Outline each Plasmodium ovale-infected red blood cell.
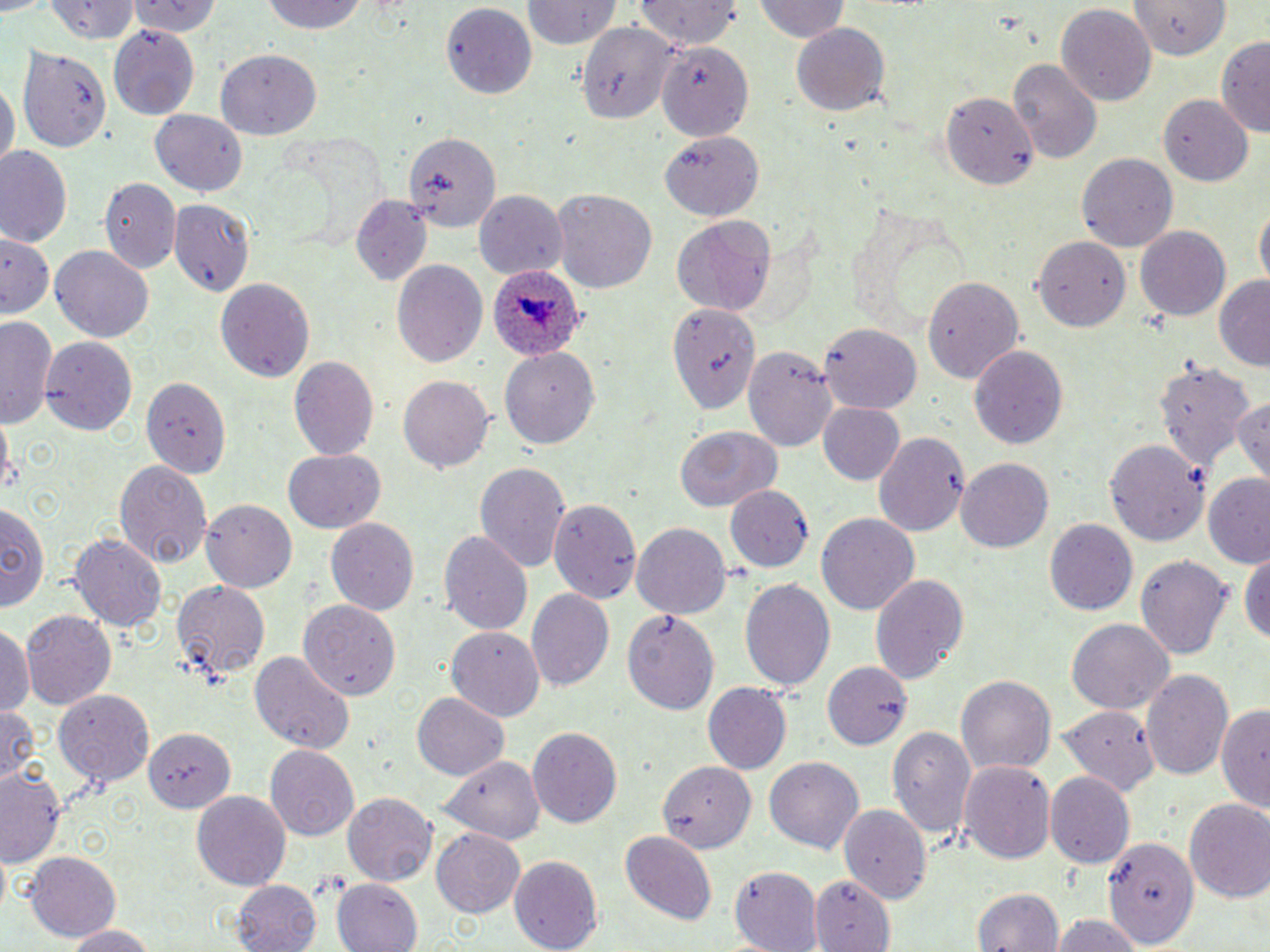
Approximate bounding boxes as named x1/y1/x2/y2 corners in pixels.
Plasmodium ovale-infected red blood cells: (x1=484, y1=264, x2=585, y2=363).

slide-level diagnosis = Plasmodium ovale
magnification = 1000x
field of view = one of a larger specimen
uninfected red blood cell locations = approximate bounding boxes as named x1/y1/x2/y2 corners in pixels: (x1=127, y1=0, x2=221, y2=37), (x1=257, y1=0, x2=371, y2=36), (x1=637, y1=0, x2=742, y2=49), (x1=754, y1=0, x2=849, y2=44), (x1=45, y1=1, x2=141, y2=44), (x1=518, y1=1, x2=622, y2=48), (x1=441, y1=3, x2=535, y2=101), (x1=1127, y1=3, x2=1233, y2=57), (x1=1055, y1=4, x2=1157, y2=103), (x1=577, y1=21, x2=677, y2=127), (x1=790, y1=21, x2=890, y2=115), (x1=107, y1=25, x2=200, y2=121), (x1=1216, y1=33, x2=1270, y2=138), (x1=656, y1=34, x2=758, y2=141), (x1=19, y1=41, x2=116, y2=152), (x1=215, y1=50, x2=319, y2=135), (x1=1009, y1=57, x2=1102, y2=164), (x1=1, y1=79, x2=15, y2=175), (x1=941, y1=92, x2=1036, y2=185), (x1=1159, y1=95, x2=1253, y2=185), (x1=151, y1=109, x2=246, y2=195), (x1=403, y1=131, x2=499, y2=234), (x1=659, y1=132, x2=762, y2=219), (x1=660, y1=134, x2=762, y2=223), (x1=1, y1=148, x2=73, y2=248), (x1=1077, y1=153, x2=1179, y2=252), (x1=100, y1=176, x2=182, y2=274), (x1=551, y1=189, x2=658, y2=294), (x1=474, y1=193, x2=565, y2=279), (x1=351, y1=194, x2=430, y2=285), (x1=170, y1=199, x2=257, y2=298), (x1=1255, y1=203, x2=1268, y2=292), (x1=672, y1=216, x2=777, y2=316), (x1=1136, y1=226, x2=1230, y2=320), (x1=1, y1=233, x2=58, y2=323), (x1=1032, y1=235, x2=1134, y2=332), (x1=51, y1=246, x2=153, y2=344), (x1=391, y1=259, x2=486, y2=370), (x1=925, y1=275, x2=1025, y2=382), (x1=215, y1=277, x2=314, y2=385), (x1=1214, y1=277, x2=1270, y2=370), (x1=668, y1=298, x2=763, y2=417), (x1=1, y1=317, x2=58, y2=428), (x1=822, y1=321, x2=924, y2=411), (x1=40, y1=335, x2=137, y2=436), (x1=740, y1=341, x2=838, y2=451), (x1=968, y1=343, x2=1067, y2=449), (x1=499, y1=349, x2=595, y2=449), (x1=290, y1=355, x2=379, y2=462), (x1=1155, y1=362, x2=1257, y2=476), (x1=139, y1=373, x2=230, y2=476), (x1=399, y1=375, x2=492, y2=473), (x1=1231, y1=392, x2=1269, y2=485), (x1=818, y1=403, x2=906, y2=486), (x1=672, y1=425, x2=781, y2=513), (x1=874, y1=431, x2=972, y2=537), (x1=1103, y1=440, x2=1206, y2=543), (x1=283, y1=451, x2=384, y2=532), (x1=114, y1=458, x2=212, y2=568), (x1=956, y1=458, x2=1055, y2=552), (x1=476, y1=460, x2=571, y2=576), (x1=1203, y1=477, x2=1270, y2=568), (x1=725, y1=486, x2=812, y2=572), (x1=551, y1=498, x2=642, y2=605), (x1=200, y1=499, x2=297, y2=592), (x1=0, y1=500, x2=49, y2=615), (x1=817, y1=513, x2=920, y2=618), (x1=326, y1=518, x2=419, y2=619), (x1=1044, y1=519, x2=1136, y2=617), (x1=632, y1=524, x2=731, y2=619), (x1=440, y1=529, x2=533, y2=638), (x1=71, y1=533, x2=167, y2=635), (x1=1241, y1=544, x2=1270, y2=650), (x1=1137, y1=552, x2=1232, y2=658), (x1=868, y1=573, x2=969, y2=688), (x1=738, y1=576, x2=834, y2=691), (x1=170, y1=580, x2=268, y2=684), (x1=525, y1=588, x2=615, y2=691), (x1=300, y1=599, x2=403, y2=695), (x1=623, y1=607, x2=718, y2=715), (x1=21, y1=611, x2=116, y2=711), (x1=1066, y1=617, x2=1174, y2=715), (x1=0, y1=624, x2=33, y2=720), (x1=448, y1=626, x2=544, y2=722), (x1=250, y1=651, x2=355, y2=755), (x1=824, y1=661, x2=913, y2=748), (x1=1142, y1=669, x2=1234, y2=784), (x1=958, y1=675, x2=1055, y2=775), (x1=703, y1=683, x2=793, y2=775), (x1=54, y1=690, x2=154, y2=790), (x1=411, y1=692, x2=510, y2=782), (x1=1217, y1=697, x2=1269, y2=809), (x1=0, y1=704, x2=44, y2=789), (x1=1060, y1=704, x2=1158, y2=796), (x1=886, y1=724, x2=975, y2=840), (x1=527, y1=726, x2=623, y2=828), (x1=143, y1=729, x2=234, y2=813), (x1=265, y1=743, x2=360, y2=837), (x1=437, y1=754, x2=537, y2=908), (x1=445, y1=757, x2=571, y2=844), (x1=766, y1=758, x2=863, y2=853), (x1=658, y1=759, x2=756, y2=853), (x1=964, y1=762, x2=1057, y2=866), (x1=0, y1=763, x2=67, y2=870), (x1=1044, y1=772, x2=1133, y2=869), (x1=192, y1=792, x2=289, y2=888), (x1=343, y1=794, x2=435, y2=886), (x1=1184, y1=799, x2=1270, y2=906), (x1=839, y1=805, x2=931, y2=906), (x1=619, y1=829, x2=717, y2=925), (x1=432, y1=830, x2=525, y2=915), (x1=1105, y1=833, x2=1198, y2=950), (x1=26, y1=852, x2=120, y2=942), (x1=508, y1=856, x2=603, y2=950), (x1=732, y1=866, x2=823, y2=950), (x1=811, y1=874, x2=894, y2=952), (x1=330, y1=878, x2=419, y2=952), (x1=230, y1=879, x2=324, y2=952), (x1=970, y1=888, x2=1067, y2=952), (x1=1050, y1=911, x2=1144, y2=952), (x1=59, y1=924, x2=156, y2=951)
preparation = thin blood smear
modality = light microscopy
image size = 1270×952 pixels
stain = May-Grünwald-Giemsa